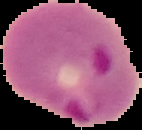

preparation = thin blood film
image type = segmented cell region on a black background
image size = 142×130 pixels
malaria status = parasitized